Describe the morphology of the erythrocytes.
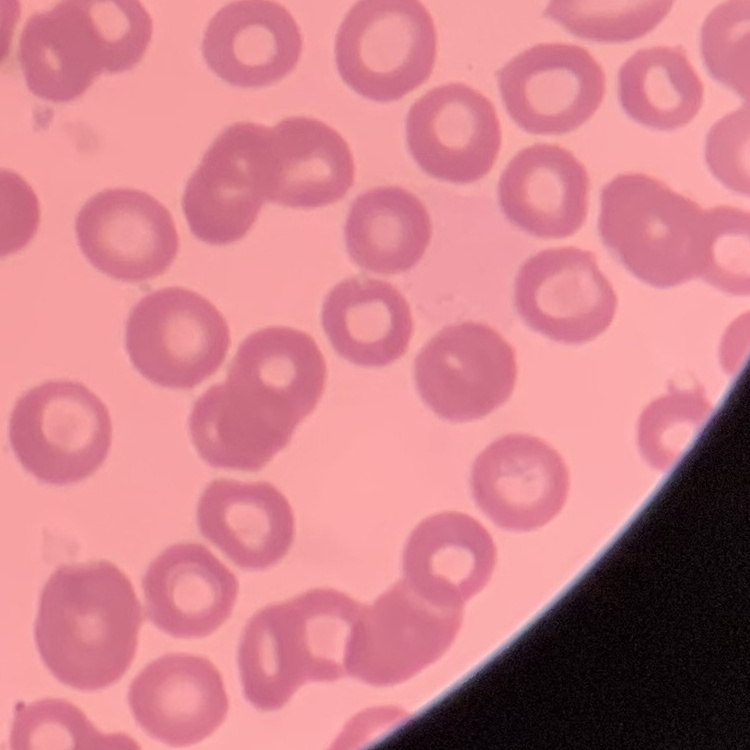

No rouleaux formation.

Stained with either Field's or Giemsa. Thin peripheral smear. One tile cut from a larger photomicrograph.